Report the malaria status of this cell.
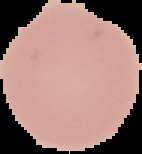

Uninfected.

Summary:
  - Image size: 142×154 pixels
  - Image type: cell region segmented out of the field of view; surrounding area masked to black
  - Preparation: thin blood film